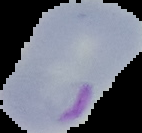
Summary:
  - Malaria status: parasitized
  - Image size: 142×133 pixels
  - Preparation: thin blood film
  - Image type: segmented cell region on a black background